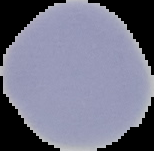

preparation = thin blood film
image type = cell region segmented out of the field of view; surrounding area masked to black
image size = 154×151 pixels
result = negative for Plasmodium parasites